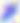

modality = photomicrograph
magnification = 400x
identification = Toxoplasma gondii